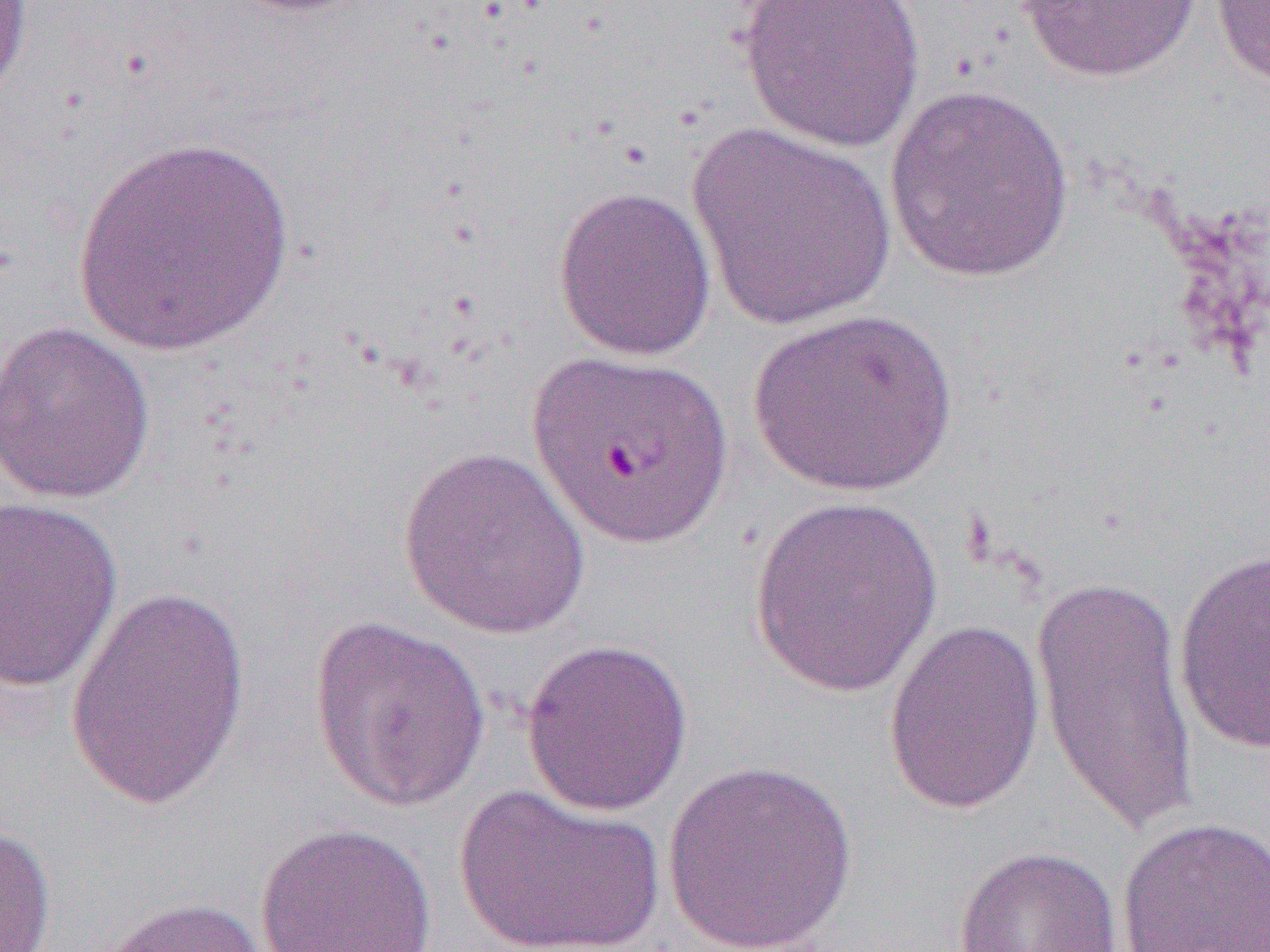
slide-level diagnosis = Plasmodium falciparum
uninfected red blood cell locations = approximate bounding boxes as named x1/y1/x2/y2 corners in pixels: (x1=0, y1=0, x2=34, y2=102), (x1=735, y1=0, x2=926, y2=154), (x1=1209, y1=0, x2=1270, y2=92), (x1=1018, y1=1, x2=1203, y2=83), (x1=883, y1=83, x2=1075, y2=283), (x1=685, y1=122, x2=898, y2=331), (x1=71, y1=133, x2=295, y2=355), (x1=552, y1=184, x2=718, y2=362), (x1=746, y1=308, x2=958, y2=497), (x1=0, y1=320, x2=157, y2=505), (x1=526, y1=349, x2=733, y2=550), (x1=397, y1=446, x2=591, y2=641), (x1=747, y1=494, x2=947, y2=697), (x1=1, y1=496, x2=123, y2=693), (x1=1172, y1=546, x2=1270, y2=755), (x1=1032, y1=567, x2=1199, y2=842), (x1=65, y1=583, x2=251, y2=812), (x1=308, y1=614, x2=492, y2=814), (x1=882, y1=617, x2=1046, y2=816), (x1=520, y1=637, x2=694, y2=817), (x1=660, y1=758, x2=859, y2=952), (x1=454, y1=782, x2=667, y2=952), (x1=1116, y1=816, x2=1270, y2=952), (x1=255, y1=821, x2=437, y2=952), (x1=0, y1=823, x2=57, y2=951), (x1=953, y1=845, x2=1122, y2=952), (x1=96, y1=896, x2=275, y2=952)
preparation = thin blood film
field of view = single
image size = 1270×952 pixels
magnification = 1000x
modality = optical microscopy